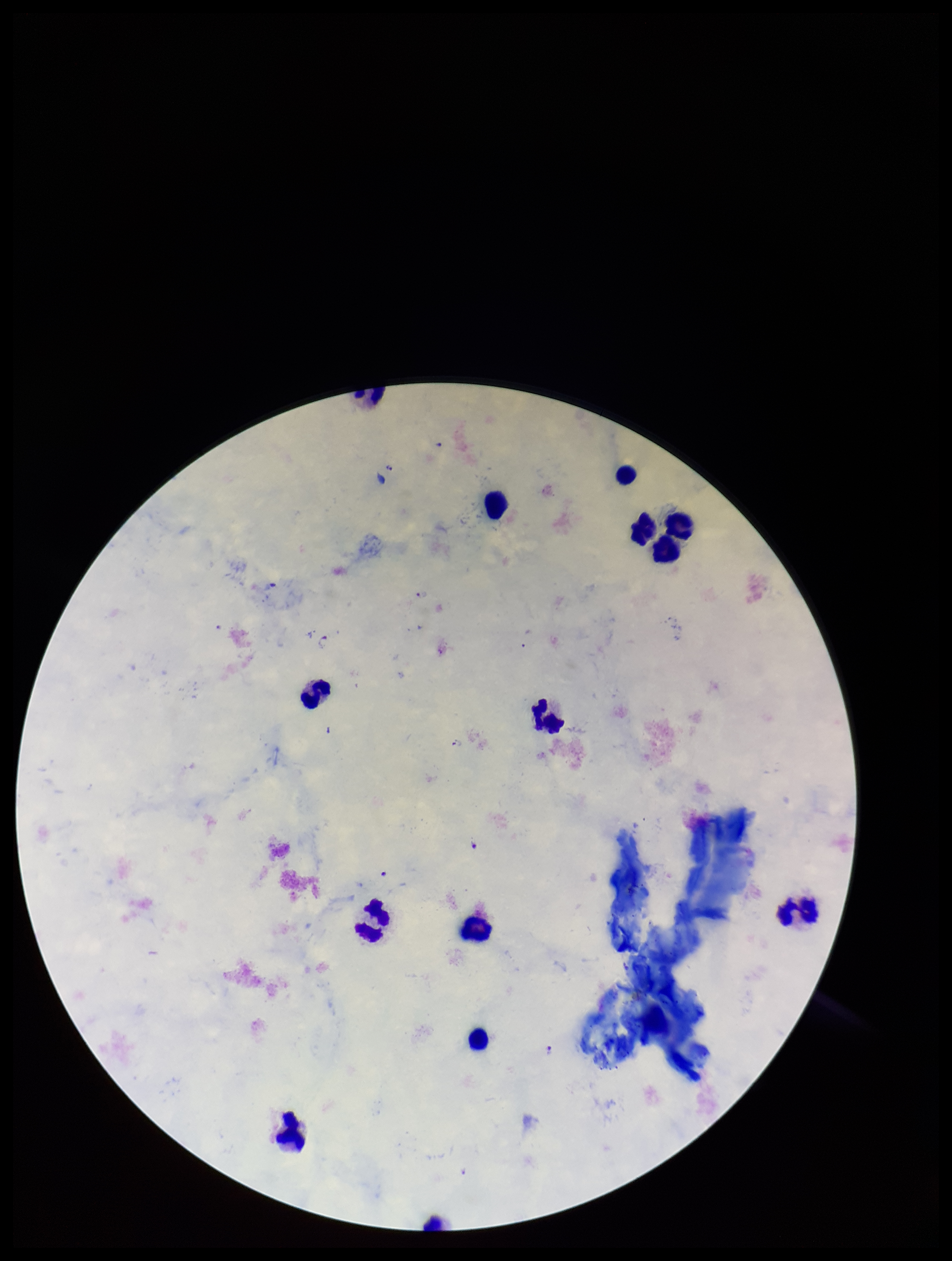
Summary:
  - Capture: smartphone photograph through the microscope eyepiece
  - Image size: 952×1261 pixels
  - Stain: Giemsa
  - Parasite count: 8
  - Patient malaria status: infected
  - Species reported for this patient: Plasmodium falciparum
  - Preparation: thick
  - Field of view: single
  - Leukocyte count: 14
  - Plasmodium parasites: detected